Identify the parasite.
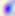
Toxoplasma gondii.

{
  "modality": "micrograph",
  "magnification": "400x"
}